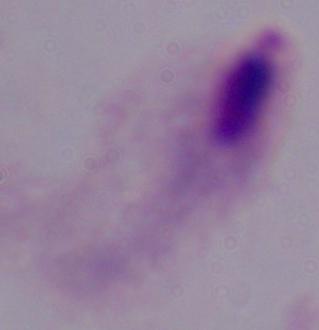
1000x magnification. Photomicrograph. A trichomonad is shown.